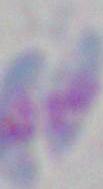

Summary:
  - Magnification: 1000x
  - Identification: Toxoplasma gondii
  - Modality: photomicrograph